Point out each Plasmodium parasite.
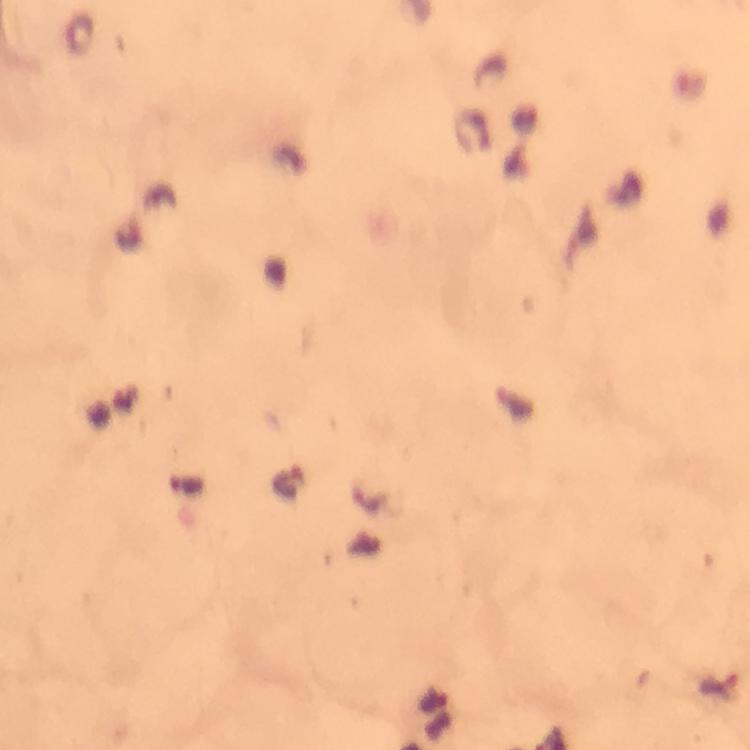

Approximate centers as [x, y] in pixels.
Plasmodium parasites: [287, 483], [717, 682].

Image is 750×750 pixels. Giemsa stain. Smartphone photograph taken through a microscope. From a diagnostic examination for malaria. 100x magnification. A crop from one field of view. Thick blood film. Immersion oil was used.